Outline each uninfected red blood cell.
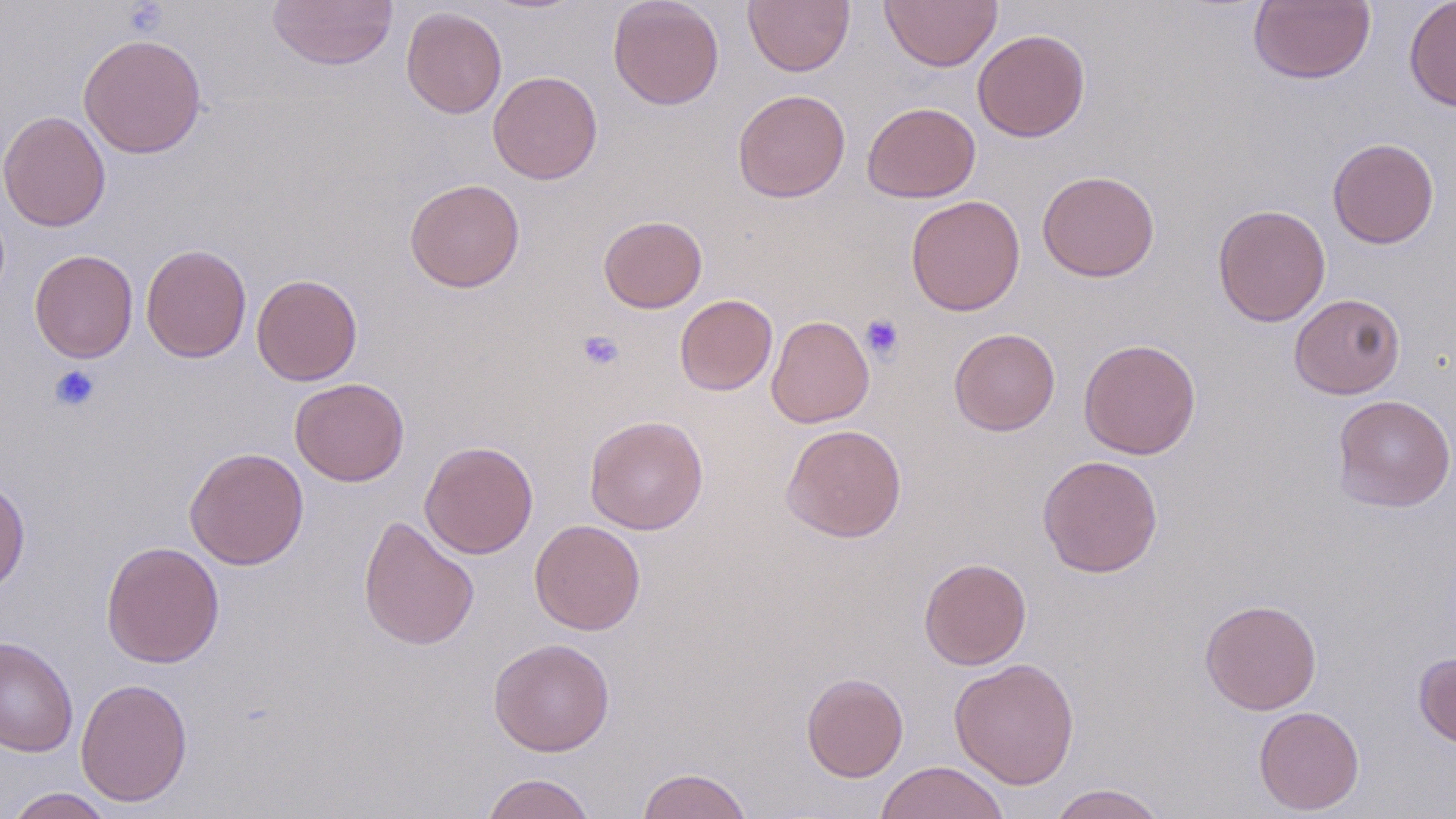

Approximate bounding boxes as (x1, y1, x2, y2) in pixels.
Uninfected red blood cells: (607, 0, 725, 110), (743, 0, 854, 75), (880, 0, 1001, 71), (1248, 0, 1376, 85), (1404, 0, 1456, 112), (266, 1, 398, 71), (401, 6, 507, 118), (972, 29, 1091, 142), (78, 33, 207, 159), (487, 70, 603, 185), (732, 89, 851, 202), (862, 102, 981, 202), (0, 110, 111, 232), (1327, 137, 1440, 249), (1036, 170, 1160, 281), (404, 178, 525, 293), (905, 194, 1025, 316), (1212, 204, 1331, 326), (598, 215, 707, 313), (141, 244, 251, 363), (29, 249, 138, 363), (251, 273, 363, 385), (1289, 293, 1405, 399), (674, 294, 778, 396), (766, 314, 874, 428), (949, 328, 1060, 435), (1078, 339, 1201, 459), (290, 377, 409, 486), (1332, 394, 1456, 513), (584, 414, 708, 535), (780, 423, 907, 542), (420, 440, 538, 559), (184, 446, 308, 570), (1037, 455, 1164, 578), (0, 477, 31, 595), (358, 514, 480, 651), (530, 519, 645, 635), (101, 541, 225, 668), (918, 557, 1032, 670), (1200, 599, 1322, 714), (0, 635, 78, 757), (488, 638, 614, 756), (1413, 652, 1456, 749), (949, 658, 1080, 789), (801, 672, 909, 782), (76, 678, 193, 807), (1253, 706, 1365, 814), (875, 761, 1011, 819), (636, 767, 754, 819), (480, 773, 595, 819), (1048, 783, 1169, 819), (3, 787, 118, 819).

Platelet locations: (860, 313, 905, 362), (576, 330, 625, 373), (48, 364, 101, 413). Slide-level diagnosis: no evidence of blood parasites. May-Grünwald-Giemsa-stained preparation. Light microscopy. Captured at 1000x magnification. Image is 1456×819 pixels. Single field of view. Thin blood smear.